Evaluate for malaria.
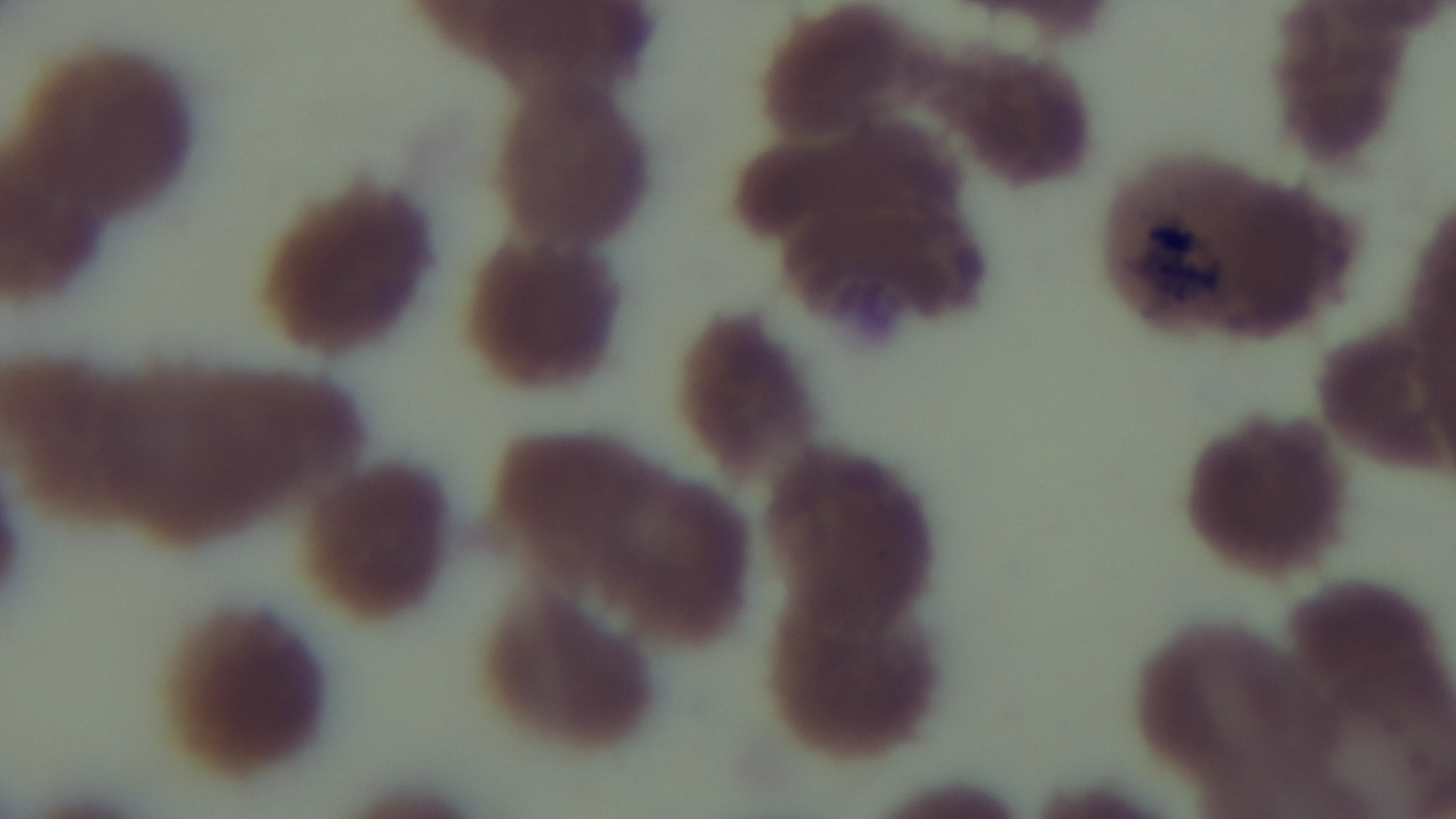

Negative.

objective = 100x oil immersion
preparation = thin
modality = light microscopy
stain = Giemsa
capture = mounted 4K digital camera
field of view = single